Classify this cell by malaria status.
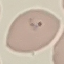

Parasitized.

Summary:
  - Preparation: thin blood smear
  - Capture: smartphone through the microscope eyepiece
  - Image type: automatically extracted cell patch, resized to 64 × 64 pixels
  - Stain: Giemsa